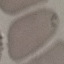
result = negative for malaria parasites
stain = Giemsa
capture = smartphone through the microscope eyepiece
preparation = thin smear
image type = automatically extracted cell patch, resized to 64 × 64 pixels